Locate and identify every blood parasite.
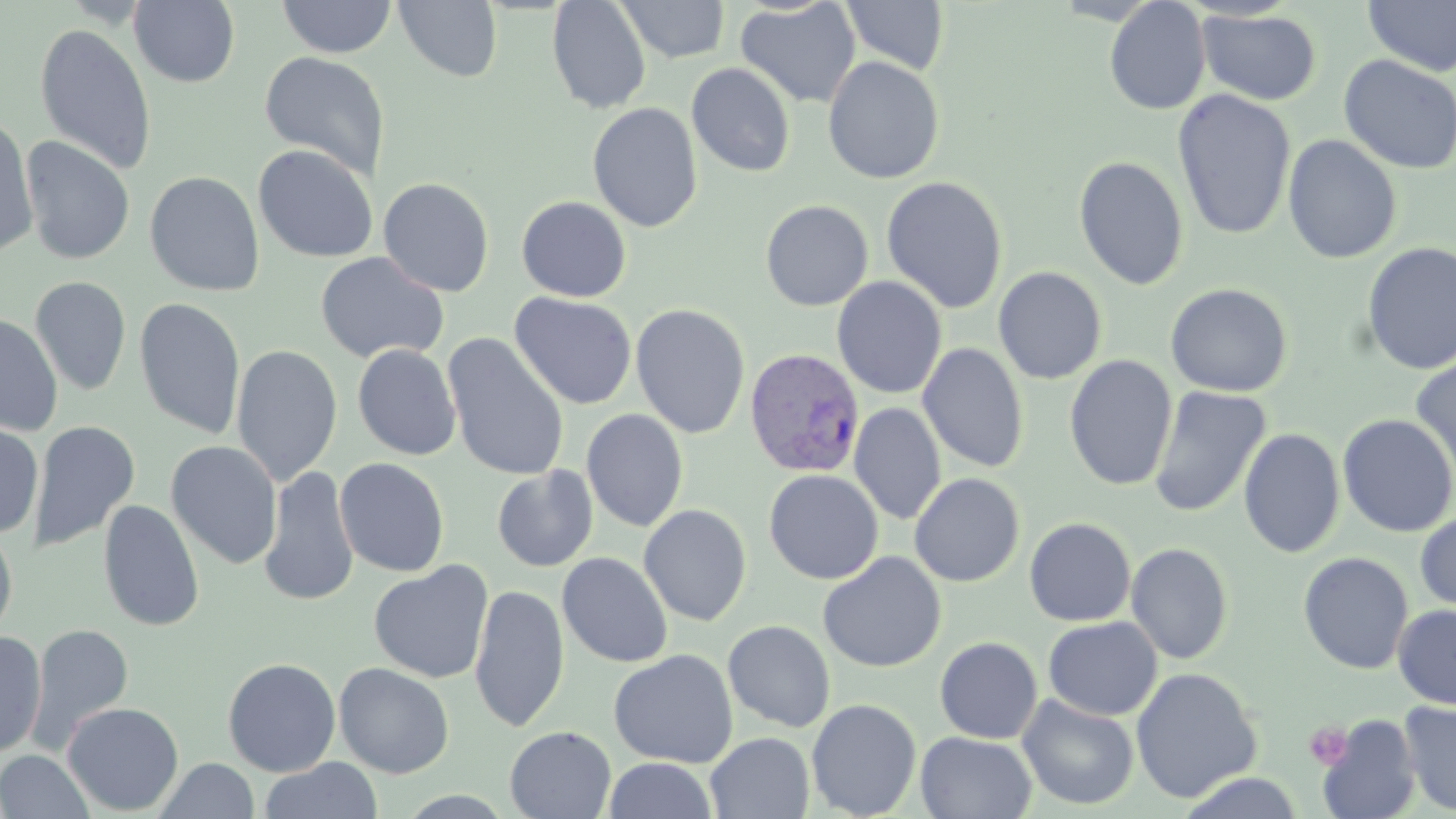
Approximate bounding boxes as [x1, y1, x2, y2] in pixels.
Plasmodium vivax-infected red blood cells: [743, 348, 867, 478].
No Plasmodium falciparum, Plasmodium ovale, Plasmodium malariae, Babesia divergens, or Trypanosoma brucei observed.

Summary:
  - Platelet locations: [1304, 721, 1354, 770]
  - Uninfected red blood cell locations: [129, 0, 240, 87], [276, 0, 397, 59], [393, 0, 503, 83], [546, 0, 651, 114], [617, 0, 730, 63], [1104, 0, 1212, 115], [1363, 0, 1456, 77], [735, 1, 861, 109], [840, 1, 949, 76], [1197, 8, 1322, 105], [33, 23, 157, 176], [258, 51, 390, 181], [1338, 54, 1455, 175], [823, 55, 945, 184], [686, 62, 796, 177], [1172, 89, 1297, 241], [587, 102, 703, 232], [0, 115, 38, 258], [1282, 134, 1402, 264], [20, 136, 136, 266], [253, 144, 378, 263], [1073, 155, 1190, 291], [144, 171, 265, 297], [881, 176, 1007, 314], [377, 177, 495, 297], [516, 196, 632, 302], [760, 200, 873, 311], [1360, 241, 1456, 376], [315, 252, 449, 364], [993, 267, 1108, 384], [832, 276, 947, 399], [30, 277, 131, 396], [1165, 283, 1293, 397], [509, 292, 637, 410], [133, 297, 246, 440], [630, 304, 750, 439], [0, 314, 62, 436], [442, 334, 570, 481], [917, 343, 1029, 473], [231, 344, 343, 486], [352, 344, 461, 461], [1409, 353, 1456, 489], [1063, 355, 1178, 491], [1148, 386, 1271, 518], [849, 403, 946, 526], [581, 409, 688, 533], [1337, 414, 1456, 537], [0, 420, 43, 538], [29, 420, 141, 553], [1238, 428, 1345, 559], [165, 440, 283, 569], [334, 458, 450, 577], [259, 465, 359, 607], [491, 465, 598, 573], [763, 469, 884, 584], [909, 473, 1025, 587], [98, 499, 205, 633], [639, 504, 752, 626], [1416, 509, 1456, 614], [1024, 517, 1136, 626], [0, 524, 18, 645], [1126, 542, 1234, 664], [1297, 551, 1414, 674], [557, 552, 673, 668], [818, 552, 946, 672], [369, 560, 494, 684], [469, 583, 569, 732], [1392, 604, 1456, 709], [1043, 616, 1162, 721], [723, 620, 836, 733], [26, 623, 134, 752], [0, 631, 47, 758], [933, 632, 1164, 733], [934, 637, 1042, 743], [608, 649, 738, 768], [222, 657, 341, 777], [334, 662, 454, 778], [1131, 667, 1262, 803], [1017, 693, 1139, 811], [806, 698, 922, 818], [61, 701, 184, 816], [1398, 701, 1456, 815], [1316, 711, 1422, 819], [504, 725, 616, 818], [705, 732, 815, 819], [915, 732, 1037, 818], [0, 750, 94, 818], [603, 756, 718, 818], [260, 757, 384, 819], [154, 758, 259, 818], [1177, 772, 1305, 818]
  - Slide-level diagnosis: Plasmodium vivax
  - Field of view: one of a larger specimen
  - Image size: 1456×819 pixels
  - Modality: light microscopy
  - Stain: May-Grünwald-Giemsa
  - Preparation: thin blood smear
  - Magnification: 1000x